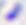

Summary:
  - Magnification: 400x
  - Identification: Toxoplasma gondii
  - Modality: photomicrograph